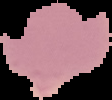
Summary:
  - Image type: cell region segmented out of the field of view; surrounding area masked to black
  - Preparation: thin blood smear
  - Image size: 112×100 pixels
  - Malaria status: parasitized